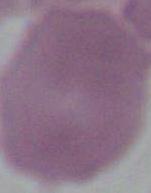

{
  "identification": "erythrocyte",
  "modality": "photomicrograph",
  "magnification": "1000x"
}